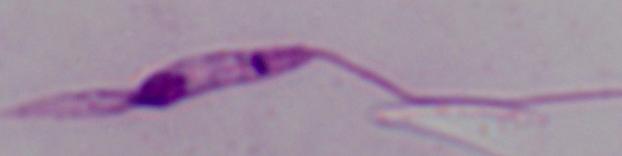
magnification = 1000x
identification = Leishmania
modality = micrograph